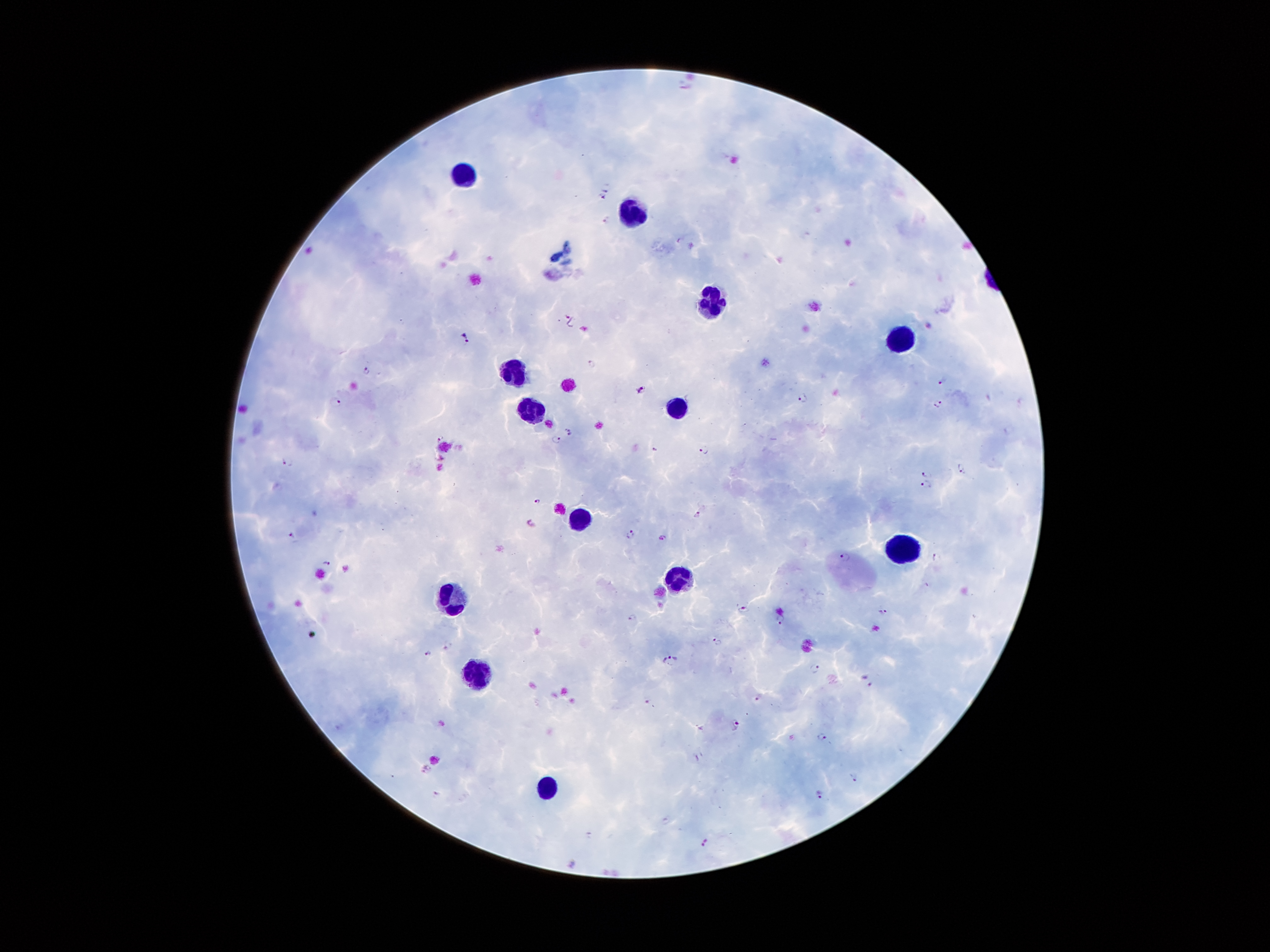

coordinate format = approximate centers as {x, y} in pixels
leukocyte locations = {460, 177}, {638, 209}, {711, 294}, {904, 336}, {518, 375}, {535, 411}, {675, 411}, {577, 513}, {898, 548}, {682, 577}, {449, 599}, {478, 672}, {545, 789}
malaria parasite locations = {607, 187}, {601, 197}, {607, 221}, {570, 319}, {464, 340}, {592, 363}, {367, 371}, {943, 381}, {644, 391}, {803, 398}, {336, 401}, {939, 405}, {569, 432}, {440, 438}, {556, 438}, {654, 449}, {705, 449}, {287, 460}, {961, 468}, {928, 474}, {925, 486}, {539, 501}, {698, 514}, {530, 523}, {630, 532}, {293, 536}, {663, 537}, {845, 556}, {937, 557}, {327, 564}, {743, 608}, {885, 611}, {632, 617}, {780, 621}, {717, 641}, {449, 645}, {428, 654}, {670, 658}, {814, 668}, {869, 681}, {758, 697}, {648, 701}, {734, 725}, {822, 737}, {426, 769}, {854, 777}, {819, 796}, {703, 843}
preparation = thick peripheral-blood smear
field of view = single
stain = Giemsa
patient malaria status = infected with Plasmodium falciparum
magnification = 100x
image size = 1270×952 pixels
capture = smartphone camera through the microscope eyepiece